Give the extent of all Plasmodium falciparum-infected red blood cells.
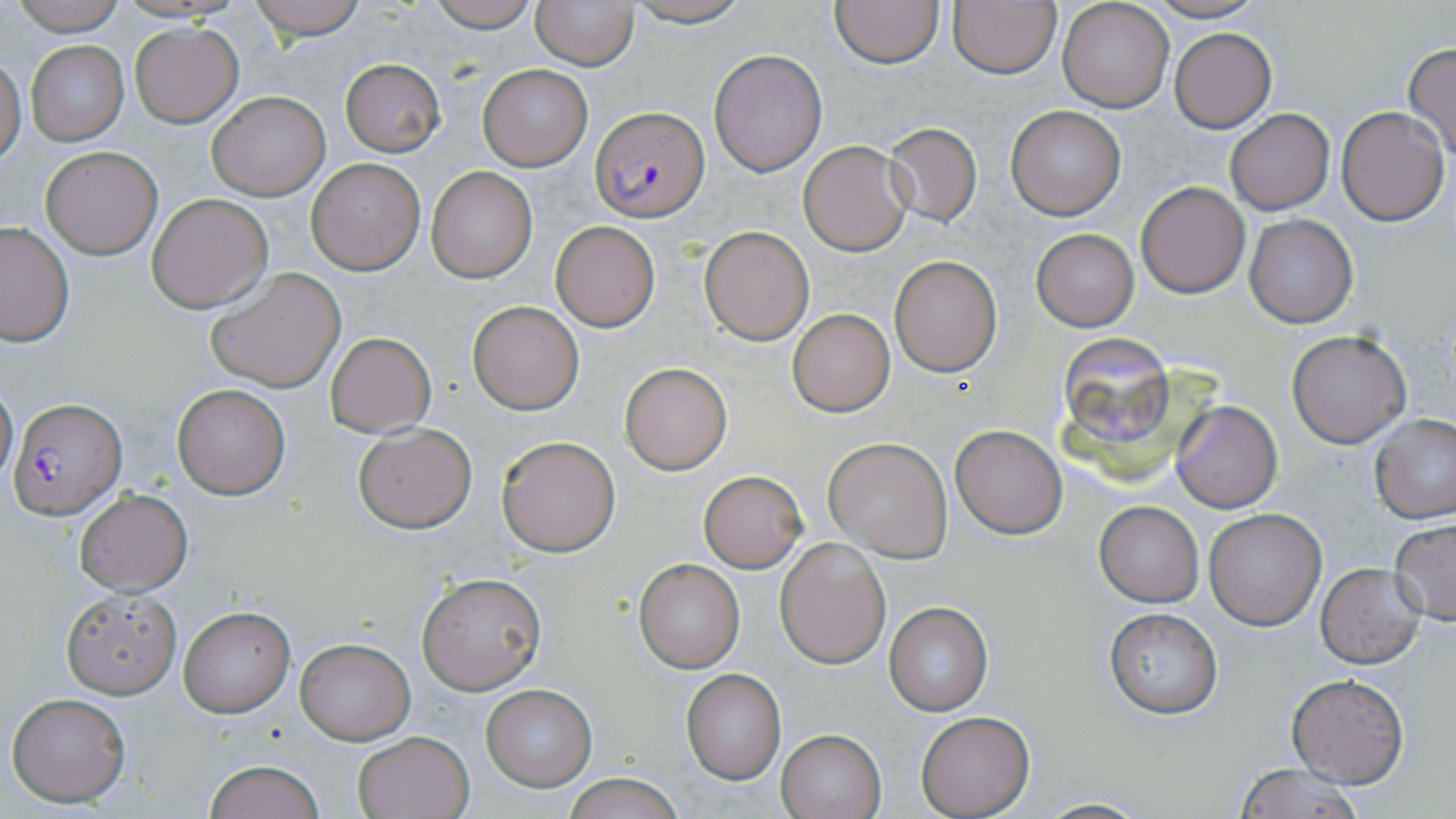
Approximate bounding boxes as [x1, y1, x2, y2] in pixels.
Plasmodium falciparum-infected red blood cells: [591, 107, 710, 222], [9, 399, 124, 516].

Uninfected red blood cell locations: [9, 0, 127, 35], [246, 0, 369, 40], [422, 0, 541, 32], [530, 0, 640, 70], [622, 0, 753, 27], [829, 0, 945, 68], [947, 0, 1062, 77], [1142, 0, 1267, 24], [1057, 2, 1173, 113], [131, 23, 242, 126], [1170, 29, 1277, 132], [27, 39, 128, 145], [1403, 43, 1456, 161], [709, 49, 827, 176], [0, 54, 25, 169], [340, 58, 445, 157], [478, 65, 592, 171], [206, 91, 327, 200], [1004, 104, 1126, 221], [1335, 106, 1450, 226], [1224, 107, 1335, 216], [884, 123, 983, 228], [798, 140, 914, 255], [40, 146, 163, 259], [305, 157, 425, 275], [425, 168, 538, 283], [1135, 181, 1251, 299], [147, 192, 274, 312], [1244, 212, 1359, 329], [551, 221, 660, 331], [0, 222, 75, 345], [699, 226, 815, 345], [1032, 228, 1138, 330], [888, 256, 1002, 376], [205, 267, 347, 394], [468, 301, 584, 414], [788, 309, 894, 416], [1286, 329, 1411, 447], [324, 331, 436, 436], [619, 362, 733, 475], [0, 376, 18, 489], [172, 384, 290, 499], [1171, 401, 1282, 512], [1368, 414, 1456, 524], [352, 423, 477, 533], [951, 425, 1068, 539], [495, 434, 620, 557], [825, 439, 952, 561], [698, 470, 806, 572], [72, 489, 192, 595], [1095, 502, 1203, 606], [1204, 509, 1326, 629], [1388, 518, 1456, 626], [774, 536, 891, 668], [633, 558, 746, 672], [1315, 562, 1426, 667], [417, 571, 546, 695], [61, 588, 181, 699], [883, 602, 994, 715], [178, 607, 295, 717], [1104, 608, 1223, 718], [294, 638, 414, 744], [679, 668, 786, 784], [1288, 674, 1408, 788], [480, 684, 597, 791], [7, 692, 131, 807], [915, 710, 1034, 817], [776, 728, 886, 819], [352, 731, 474, 819], [203, 759, 326, 819], [1232, 763, 1371, 817], [562, 773, 685, 819], [1027, 797, 1151, 818]. Slide-level diagnosis: Plasmodium falciparum. Thin blood smear. Single field of view. Image is 1456×819 pixels. Captured at 1000x magnification. Optical microscopy. May-Grünwald-Giemsa stain.